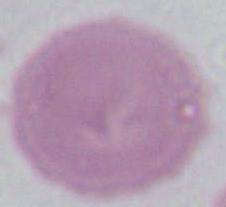

Photomicrograph. 1000x magnification. An erythrocyte is shown.